Describe the morphology of the erythrocytes.
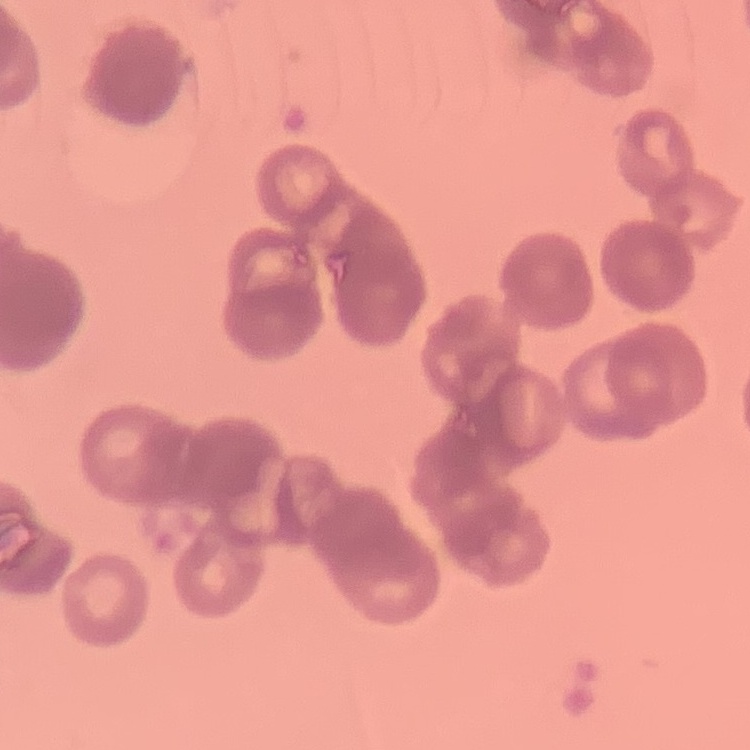

They show rouleaux formation.

Summary:
  - Image type: one tile cut from a larger photomicrograph
  - Stain: Field's or Giemsa
  - Preparation: thin blood film